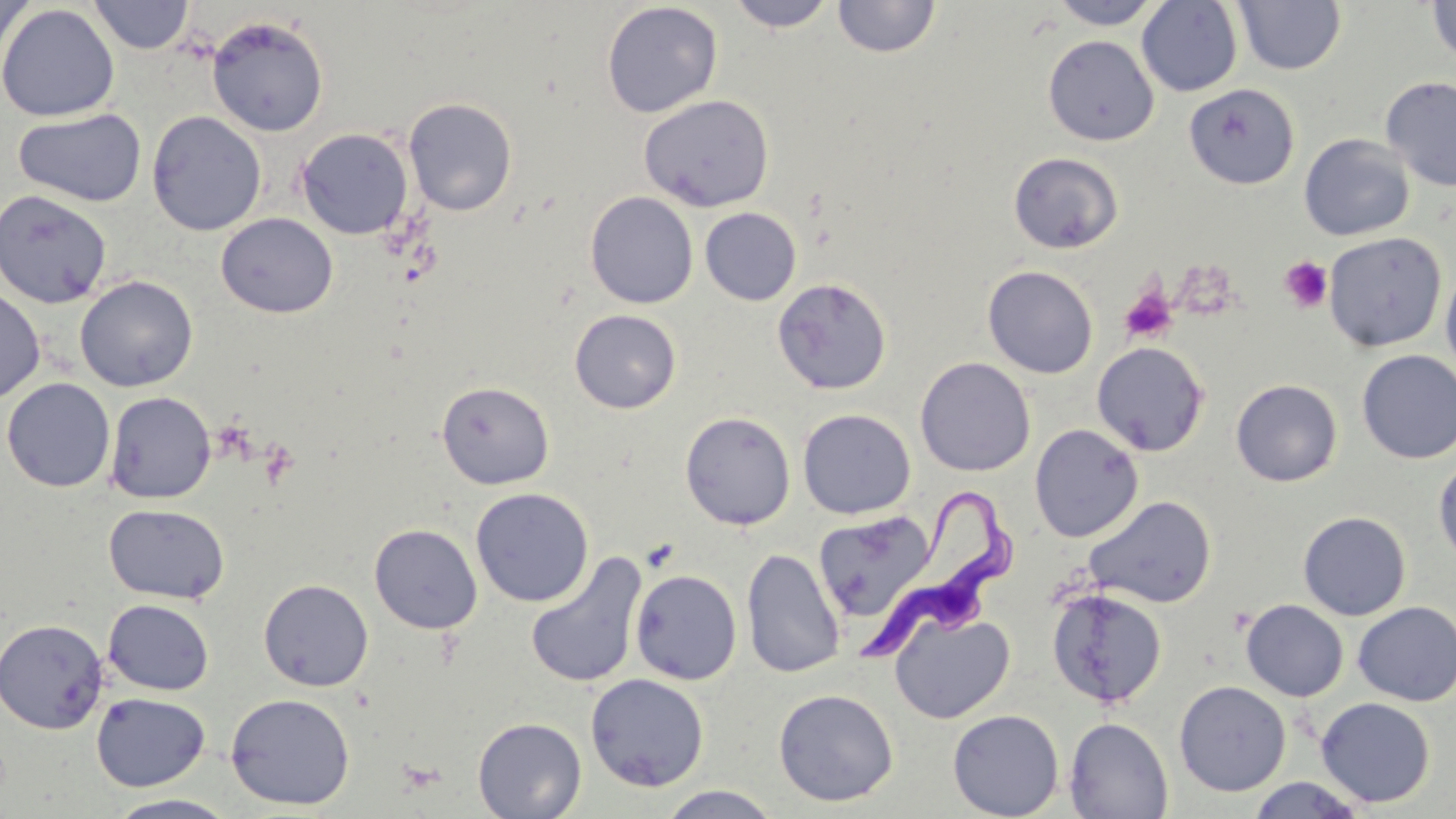

slide-level diagnosis = Trypanosoma brucei
preparation = thin blood film
magnification = 1000x
image size = 1456×819 pixels
modality = optical microscopy
Trypanosoma brucei locations = approximate bounding boxes as (x1, y1, x2, y2) in pixels: (859, 479, 1015, 671)
field of view = one of a larger specimen
stain = May-Grünwald-Giemsa
uninfected red blood cell locations = approximate bounding boxes as (x1, y1, x2, y2) in pixels: (0, 0, 33, 73), (88, 0, 194, 54), (724, 0, 839, 32), (833, 0, 941, 59), (1048, 0, 1164, 29), (1426, 0, 1456, 64), (601, 1, 723, 118), (1137, 1, 1242, 97), (1234, 1, 1346, 75), (0, 3, 119, 122), (206, 15, 329, 137), (1042, 34, 1159, 146), (1381, 75, 1456, 192), (1183, 83, 1300, 190), (638, 94, 775, 212), (403, 97, 518, 217), (13, 107, 147, 207), (146, 110, 267, 236), (296, 127, 414, 240), (1299, 134, 1415, 241), (1008, 151, 1124, 254), (0, 189, 113, 309), (585, 191, 698, 309), (700, 207, 802, 306), (215, 213, 338, 318), (1323, 232, 1447, 352), (982, 265, 1098, 379), (1440, 265, 1456, 379), (75, 275, 198, 392), (772, 277, 892, 395), (0, 284, 46, 405), (568, 309, 682, 414), (1091, 342, 1210, 456), (1356, 350, 1456, 464), (916, 357, 1035, 476), (1, 377, 116, 492), (1230, 378, 1343, 487), (436, 381, 554, 490), (104, 391, 216, 504), (797, 408, 916, 519), (679, 411, 796, 530), (1029, 424, 1143, 542), (1433, 455, 1456, 568), (470, 487, 594, 607), (1084, 495, 1217, 608), (104, 503, 230, 604), (812, 510, 939, 624), (1298, 511, 1411, 620), (369, 523, 483, 634), (740, 548, 846, 678), (524, 552, 648, 689), (630, 569, 742, 685), (258, 578, 374, 692), (1047, 587, 1167, 708), (103, 599, 215, 696), (1241, 599, 1348, 701), (1352, 601, 1456, 706), (890, 609, 1014, 724), (0, 618, 109, 734), (585, 673, 709, 792), (1174, 680, 1291, 796), (773, 688, 899, 807), (90, 692, 211, 792), (225, 692, 356, 811), (1316, 697, 1436, 808), (947, 709, 1064, 819), (1064, 716, 1174, 818), (472, 717, 587, 819), (1246, 776, 1369, 818), (656, 785, 785, 819), (105, 793, 240, 818)
platelet locations = approximate bounding boxes as (x1, y1, x2, y2) in pixels: (1279, 256, 1333, 313), (1119, 287, 1178, 344)